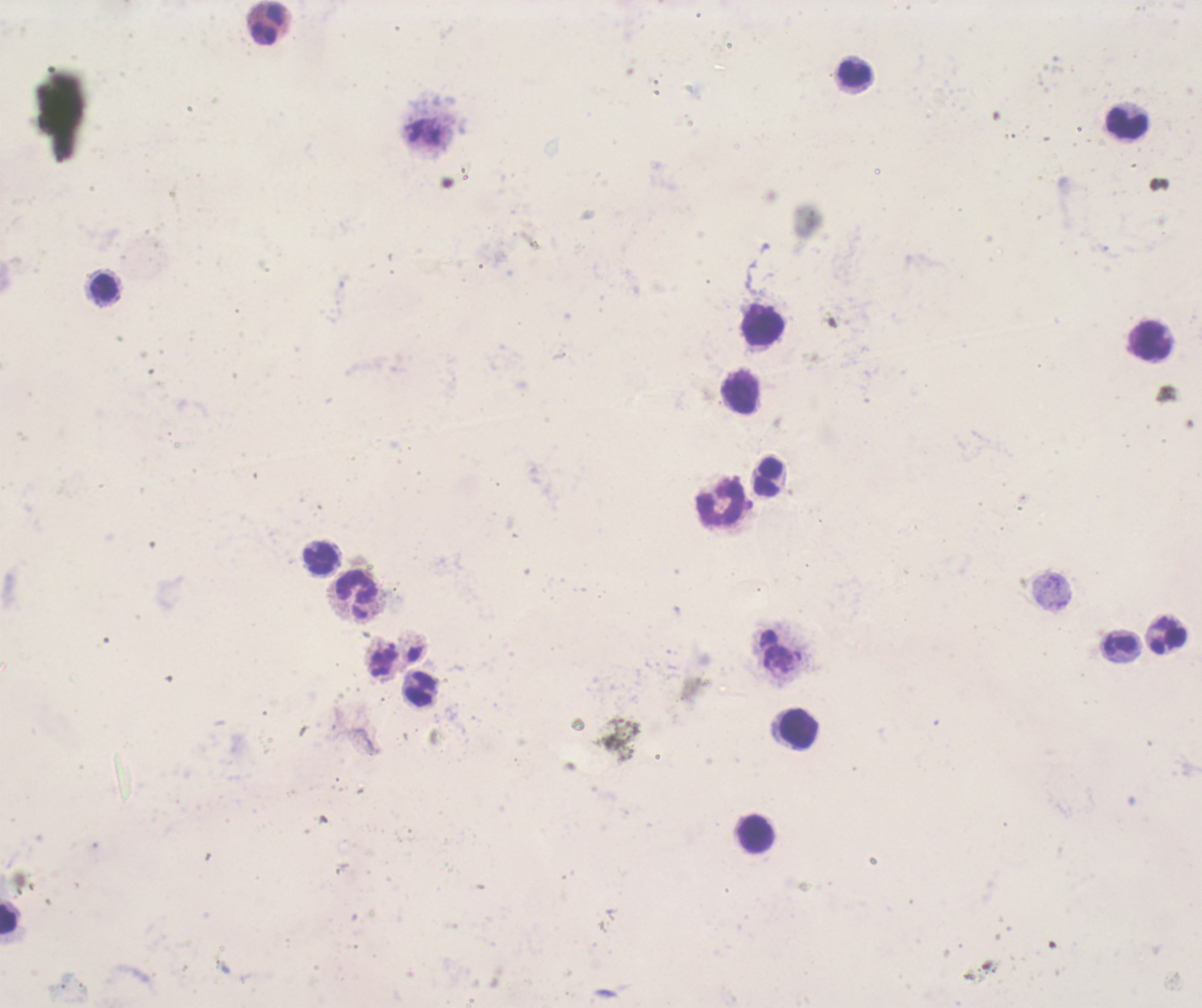
coordinate format = approximate centers as [x, y] in pixels
leukocyte locations = [269, 23], [853, 72], [1126, 124], [103, 288], [763, 325], [1149, 341], [742, 393], [769, 477], [721, 501], [321, 558], [358, 595], [1120, 644], [420, 689], [797, 727], [754, 833], [8, 919]
background quality = poor
result = no malaria parasites seen
context = previously used in a real diagnosis
coloration quality = bad
magnification = 100x
stain = Romanowsky
image size = 1202×1008 pixels
field of view = single
preparation = thick blood smear